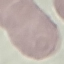
Summary:
  - Malaria status: uninfected
  - Capture: smartphone through the microscope eyepiece
  - Image type: cell patch, automatically extracted from a larger field of view and resized to 64 × 64 pixels
  - Stain: Giemsa
  - Preparation: thin blood film